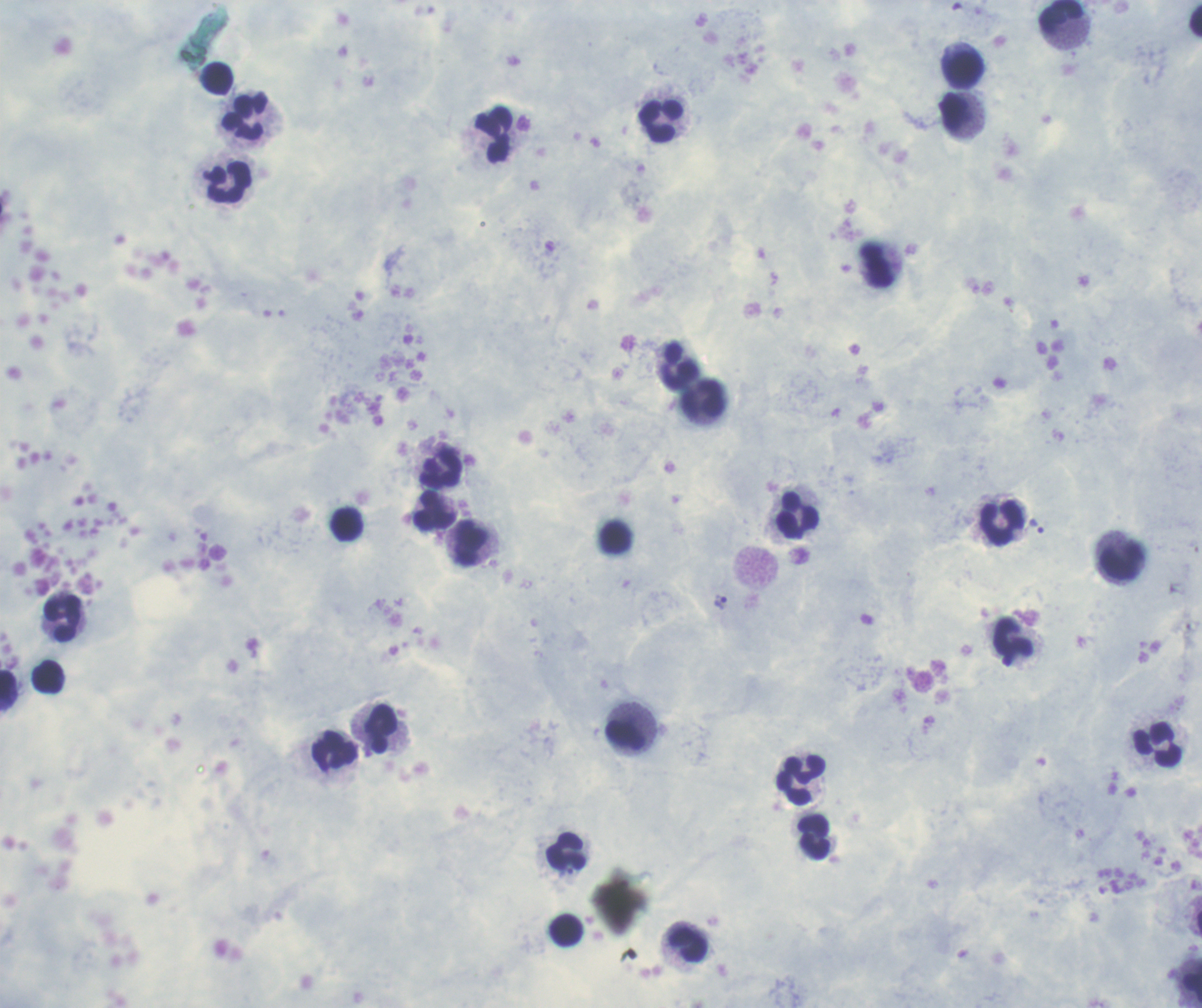

Coloration quality: good. Image is 1202×1008 pixels. One field from this slide. Thick blood film. Romanowsky-stained preparation.